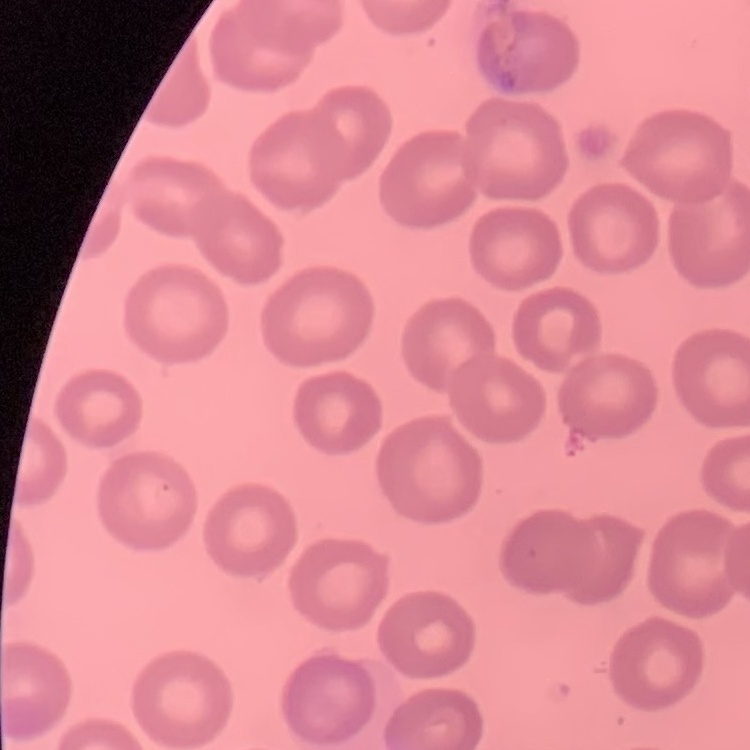 The erythrocytes exhibit no rouleaux formation. Field's or Giemsa stain. Thin peripheral smear. Square crop of a larger photomicrograph.